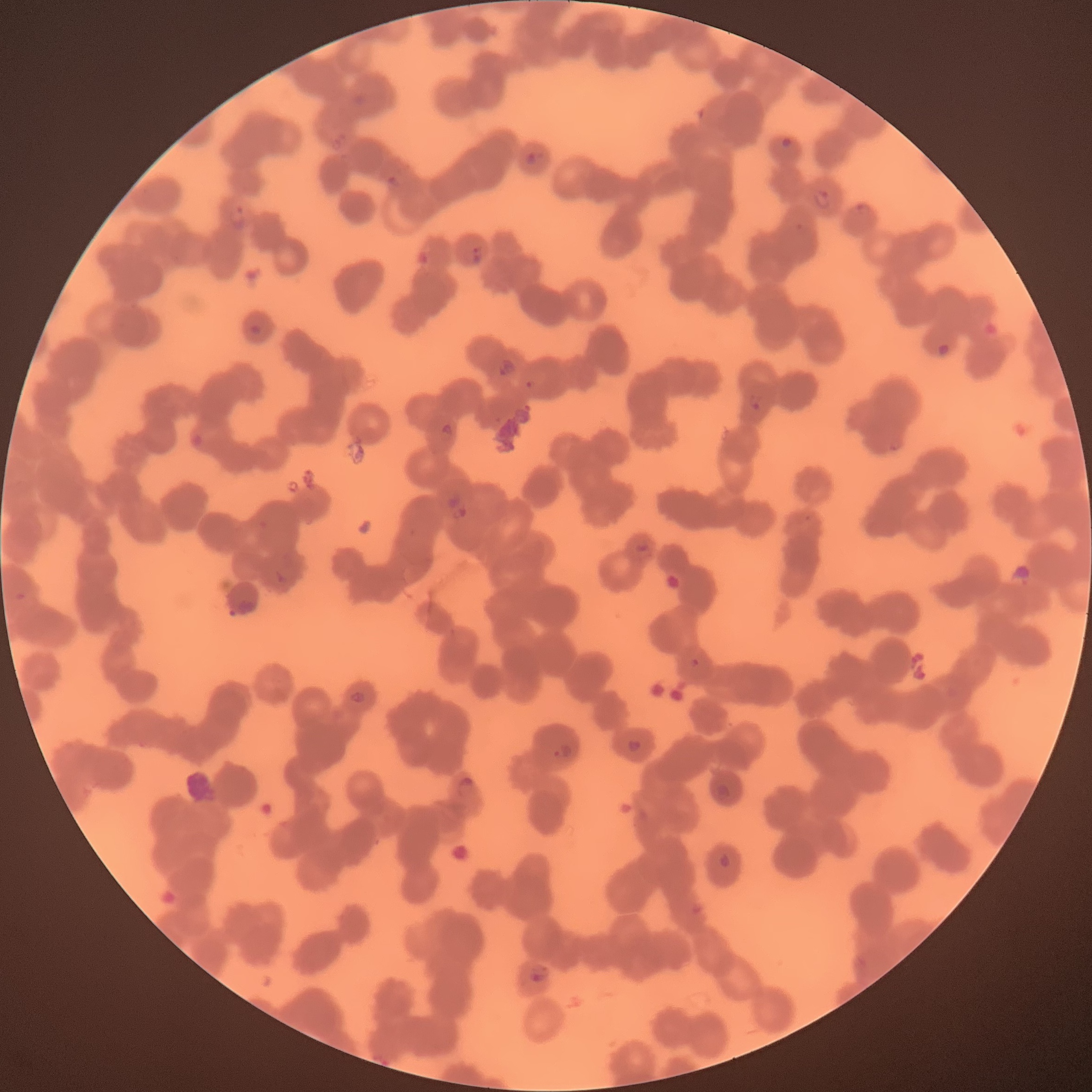

Summary:
  - Coordinate format: approximate bounding boxes as named x1/y1/x2/y2 corners in pixels
  - Plasmodium parasite locations: (x1=329, y1=129, x2=348, y2=151), (x1=781, y1=137, x2=792, y2=151), (x1=526, y1=150, x2=538, y2=166), (x1=383, y1=175, x2=401, y2=191), (x1=812, y1=188, x2=832, y2=209), (x1=855, y1=202, x2=872, y2=218), (x1=226, y1=206, x2=249, y2=233), (x1=471, y1=246, x2=485, y2=264), (x1=248, y1=323, x2=263, y2=336), (x1=936, y1=341, x2=950, y2=358), (x1=495, y1=357, x2=517, y2=379), (x1=523, y1=379, x2=538, y2=392), (x1=747, y1=394, x2=762, y2=411), (x1=435, y1=423, x2=454, y2=444), (x1=190, y1=433, x2=203, y2=447), (x1=446, y1=493, x2=467, y2=521), (x1=634, y1=542, x2=654, y2=562), (x1=229, y1=598, x2=258, y2=617), (x1=689, y1=656, x2=701, y2=667), (x1=350, y1=690, x2=366, y2=705), (x1=626, y1=738, x2=644, y2=753), (x1=552, y1=742, x2=573, y2=760), (x1=456, y1=777, x2=476, y2=798), (x1=714, y1=783, x2=731, y2=800), (x1=718, y1=852, x2=732, y2=869), (x1=529, y1=966, x2=548, y2=986)
  - Preparation: thin blood smear
  - Red blood cell morphology: rouleaux formation
  - Modality: optical microscopy
  - Image size: 1092×1092 pixels